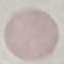

Result: negative for malaria parasites. Thin blood film. Cell patch, automatically extracted from a larger field of view and resized to 64 × 64 pixels. Acquired by smartphone through the microscope eyepiece. Giemsa-stained preparation.